Point out Plasmodium parasites and leukocytes.
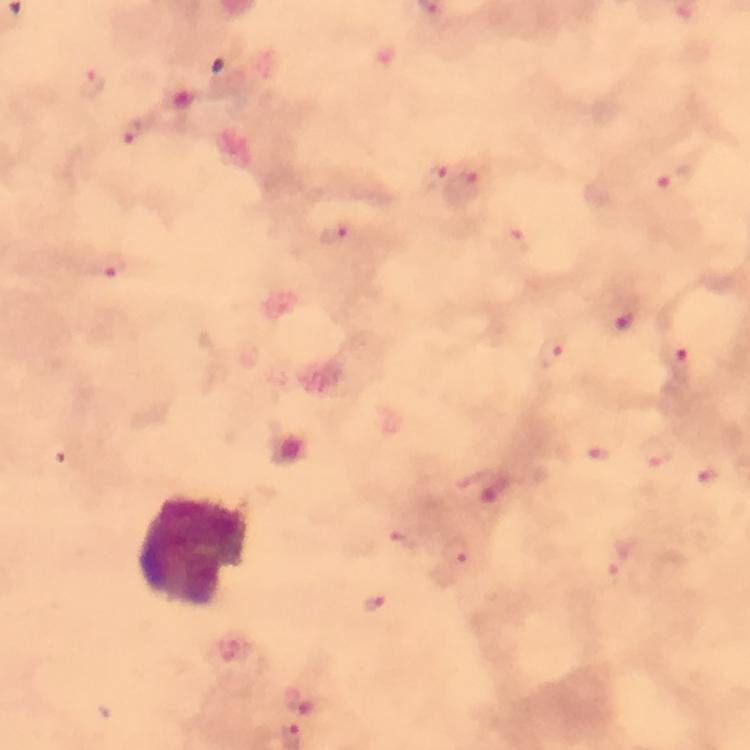

Approximate object centers, in pixels from the top-left corner.
Plasmodium parasites: (x=687, y=13), (x=434, y=176), (x=674, y=179), (x=462, y=186), (x=338, y=233), (x=512, y=241), (x=624, y=318), (x=553, y=351), (x=680, y=356), (x=658, y=453), (x=599, y=455), (x=708, y=472), (x=403, y=542), (x=456, y=552), (x=621, y=559), (x=373, y=601).
Leukocytes: (x=191, y=551).

A crop from one field of view. Thick blood smear. Image is 750×750 pixels. Photographed through the microscope with a smartphone camera. Immersion oil was used. From a malaria diagnostic workup. 100x magnification. Giemsa-stained preparation.